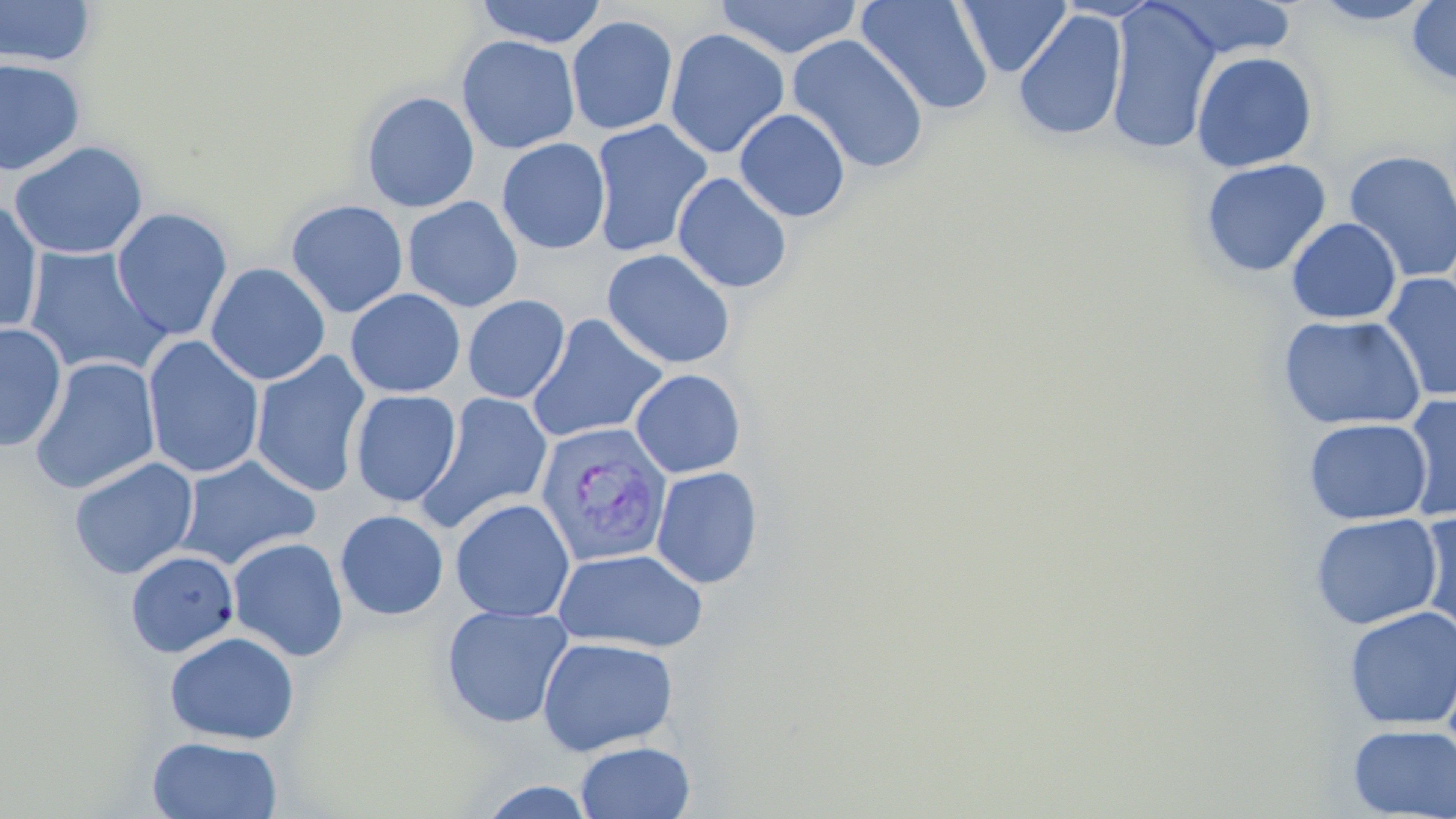

slide-level diagnosis = Plasmodium vivax
stain = May-Grünwald-Giemsa
image size = 1456×819 pixels
preparation = thin blood film
modality = light microscopy
Plasmodium vivax-infected red blood cell locations = approximate bounding boxes as named x1/y1/x2/y2 corners in pixels: (x1=534, y1=422, x2=673, y2=567)
field of view = one of a larger specimen
magnification = 1000x
uninfected red blood cell locations = approximate bounding boxes as named x1/y1/x2/y2 corners in pixels: (x1=0, y1=0, x2=97, y2=67), (x1=474, y1=0, x2=606, y2=48), (x1=713, y1=0, x2=863, y2=59), (x1=856, y1=0, x2=994, y2=117), (x1=955, y1=0, x2=1071, y2=78), (x1=1105, y1=0, x2=1222, y2=155), (x1=1155, y1=0, x2=1297, y2=59), (x1=1406, y1=0, x2=1455, y2=90), (x1=1309, y1=1, x2=1436, y2=27), (x1=1013, y1=10, x2=1128, y2=143), (x1=566, y1=15, x2=679, y2=135), (x1=665, y1=28, x2=789, y2=160), (x1=787, y1=34, x2=929, y2=174), (x1=456, y1=35, x2=580, y2=154), (x1=1191, y1=50, x2=1318, y2=173), (x1=0, y1=58, x2=86, y2=176), (x1=361, y1=91, x2=480, y2=213), (x1=734, y1=108, x2=850, y2=222), (x1=589, y1=119, x2=712, y2=258), (x1=496, y1=138, x2=611, y2=255), (x1=9, y1=140, x2=149, y2=261), (x1=1343, y1=148, x2=1456, y2=283), (x1=1199, y1=158, x2=1331, y2=278), (x1=672, y1=172, x2=793, y2=294), (x1=403, y1=196, x2=523, y2=313), (x1=285, y1=199, x2=409, y2=319), (x1=0, y1=201, x2=44, y2=337), (x1=110, y1=207, x2=233, y2=341), (x1=1287, y1=217, x2=1401, y2=324), (x1=22, y1=245, x2=171, y2=378), (x1=601, y1=248, x2=737, y2=370), (x1=206, y1=262, x2=331, y2=386), (x1=1381, y1=271, x2=1456, y2=402), (x1=345, y1=288, x2=466, y2=398), (x1=462, y1=294, x2=570, y2=403), (x1=526, y1=313, x2=668, y2=444), (x1=1277, y1=314, x2=1426, y2=431), (x1=0, y1=322, x2=67, y2=453), (x1=142, y1=335, x2=265, y2=480), (x1=249, y1=351, x2=372, y2=499), (x1=29, y1=356, x2=160, y2=495), (x1=630, y1=369, x2=746, y2=478), (x1=350, y1=389, x2=461, y2=507), (x1=417, y1=392, x2=554, y2=532), (x1=1400, y1=393, x2=1456, y2=522), (x1=1304, y1=417, x2=1431, y2=525), (x1=175, y1=455, x2=321, y2=570), (x1=69, y1=457, x2=198, y2=580), (x1=651, y1=466, x2=763, y2=590), (x1=450, y1=498, x2=576, y2=623), (x1=335, y1=509, x2=449, y2=620), (x1=1416, y1=510, x2=1456, y2=641), (x1=1310, y1=513, x2=1442, y2=630), (x1=227, y1=536, x2=349, y2=662), (x1=553, y1=548, x2=709, y2=653), (x1=125, y1=550, x2=239, y2=658), (x1=440, y1=604, x2=574, y2=729), (x1=1343, y1=605, x2=1456, y2=730), (x1=164, y1=631, x2=300, y2=745), (x1=536, y1=637, x2=678, y2=756), (x1=1347, y1=722, x2=1456, y2=818), (x1=146, y1=735, x2=283, y2=818), (x1=575, y1=741, x2=695, y2=819), (x1=478, y1=780, x2=598, y2=817)